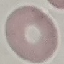
Malaria status: uninfected. Acquired by smartphone through the microscope eyepiece. Giemsa stain. Thin blood film. Automatically extracted cell patch, resized to 64 × 64 pixels.